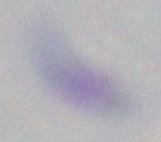

modality = micrograph
magnification = 1000x
identification = Toxoplasma gondii